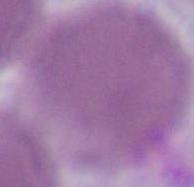

An erythrocyte is shown. Captured at 1000x magnification. Photomicrograph.